Give the preparation type.
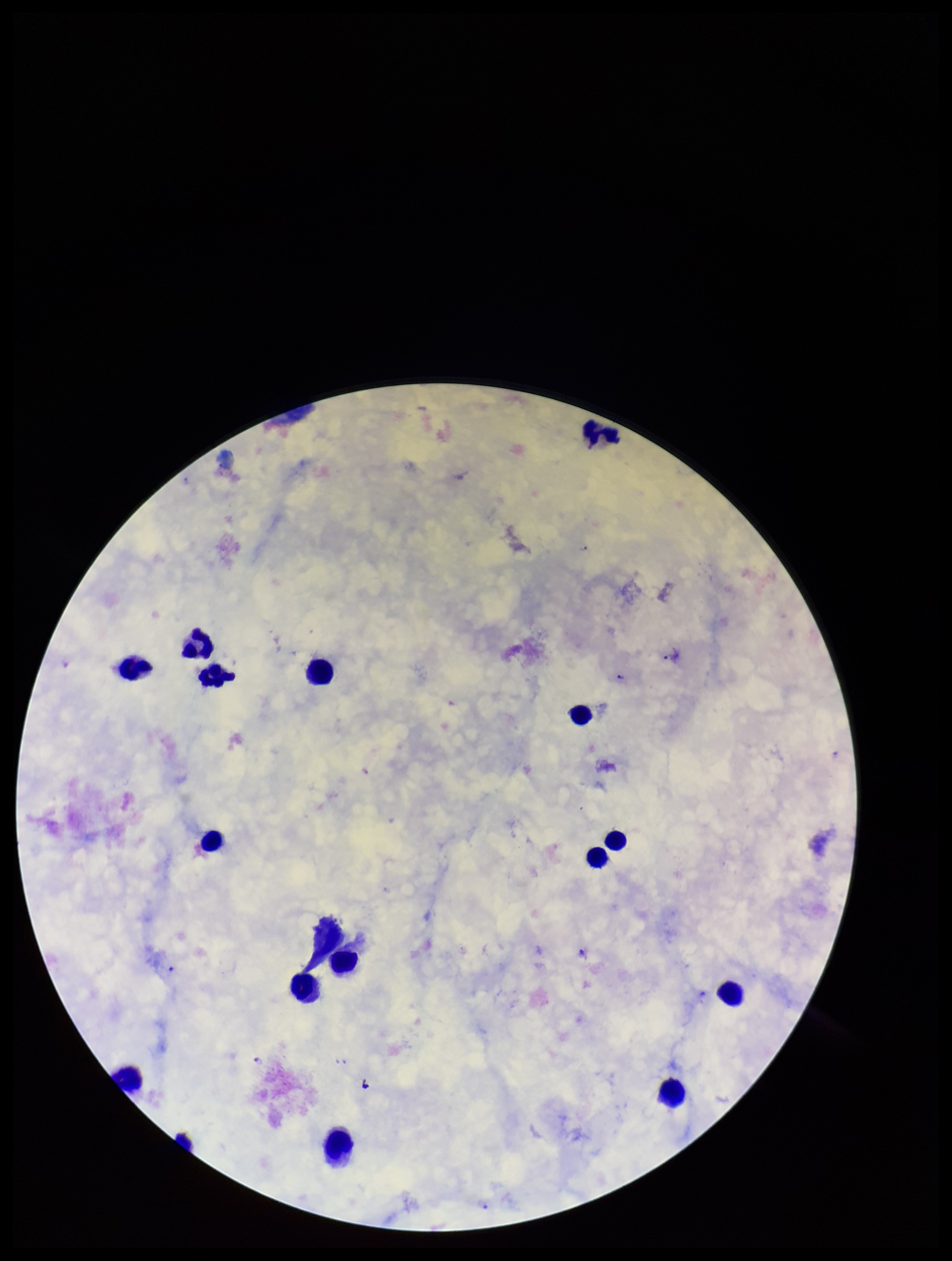
It is a thick blood smear.

Summary:
  - Capture: smartphone photograph through the microscope eyepiece
  - Patient malaria status: positive
  - Parasite count: 3
  - Leukocyte count: 15
  - Plasmodium parasites: detected
  - Image size: 952×1261 pixels
  - Field of view: one from this slide
  - Species reported for this patient: Plasmodium falciparum
  - Stain: Giemsa